Report the malaria status of this cell.
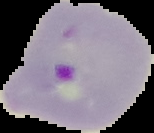

Parasitized.

The area outside the segmented cell region is set to black. From a thin blood film. Image is 154×133 pixels.